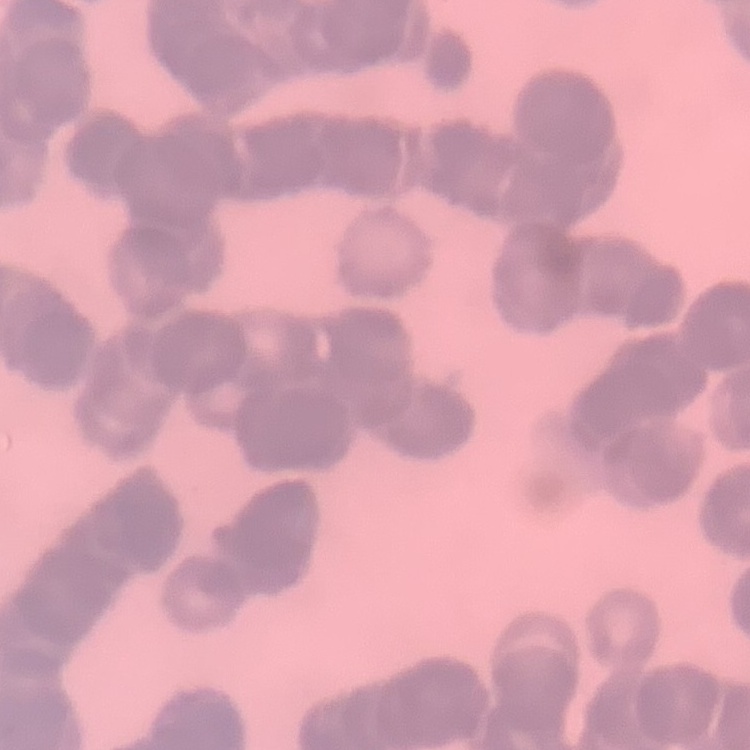

red_blood_cell_morphology: rouleaux formation
image_type: square crop of a larger photomicrograph
preparation: thin blood smear
stain: Field's or Giemsa